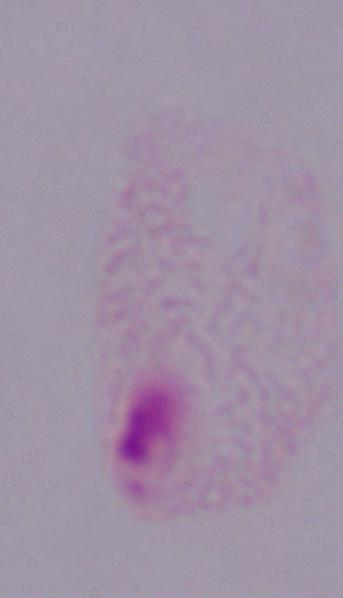

Summary:
  - Modality: micrograph
  - Identification: trichomonad
  - Magnification: 1000x